Report the malaria status of this cell.
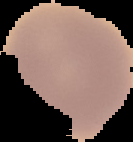

Uninfected.

Image is 133×142 pixels. Segmented cell region on a black background. From a thin blood film.